Outline each uninfected red blood cell.
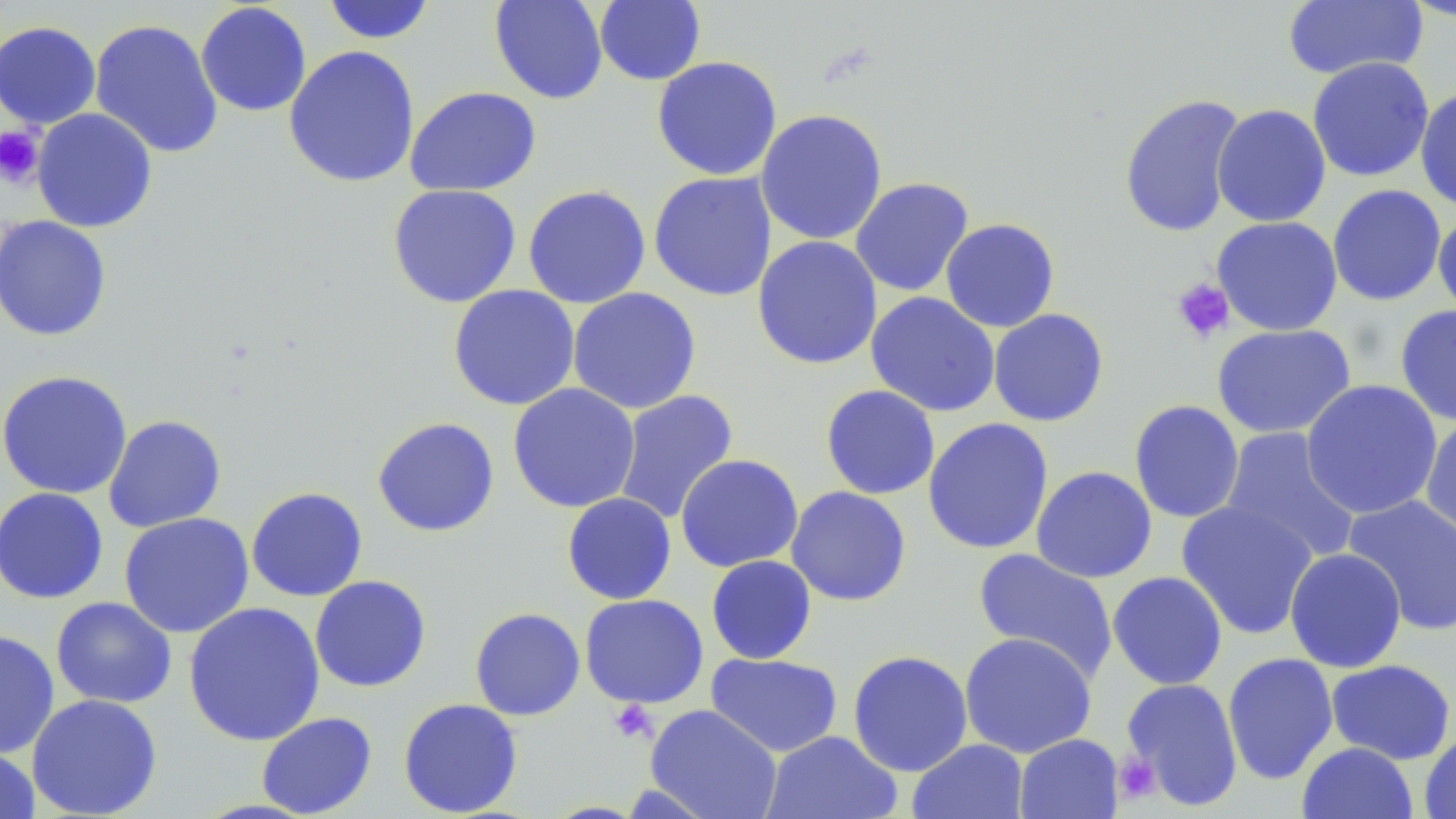

Approximate bounding boxes as (x1,y1)-(x2,y2) corner pairs in pixels.
Uninfected red blood cells: (321,0)-(437,44), (489,0)-(609,104), (595,0)-(706,85), (1398,0)-(1456,22), (1282,1)-(1427,81), (195,2)-(312,117), (89,18)-(224,159), (0,21)-(101,129), (283,45)-(420,189), (651,56)-(783,181), (1307,56)-(1434,183), (404,86)-(541,196), (1415,87)-(1456,213), (1118,93)-(1246,239), (1212,104)-(1331,227), (31,108)-(158,233), (755,109)-(888,246), (648,171)-(777,302), (849,177)-(974,297), (387,183)-(522,308), (1327,184)-(1447,306), (522,185)-(651,309), (1432,212)-(1456,320), (0,215)-(112,342), (1211,215)-(1343,336), (940,218)-(1060,332), (752,235)-(883,370), (448,285)-(580,411), (567,287)-(702,414), (865,291)-(1001,417), (1394,305)-(1456,426), (988,308)-(1109,427), (1211,323)-(1356,439), (0,370)-(133,500), (1300,379)-(1443,519), (507,383)-(641,513), (820,384)-(941,500), (613,389)-(739,525), (1129,399)-(1245,523), (103,414)-(227,533), (1420,414)-(1456,542), (371,416)-(500,537), (923,417)-(1054,555), (1219,427)-(1362,564), (675,454)-(804,573), (1031,465)-(1157,583), (246,486)-(368,602), (786,486)-(912,606), (0,487)-(109,605), (561,492)-(677,605), (1342,494)-(1456,636), (1176,500)-(1319,640), (118,512)-(255,638), (972,547)-(1120,682), (1284,548)-(1407,672), (705,555)-(817,664), (1107,571)-(1228,690), (309,575)-(432,693), (579,594)-(709,708), (51,596)-(177,708), (183,602)-(325,746), (469,607)-(586,721), (0,629)-(60,759), (959,632)-(1097,758), (847,649)-(973,777), (1222,652)-(1339,785), (705,653)-(843,758), (1325,659)-(1456,764), (1120,677)-(1244,811), (26,694)-(163,818), (398,698)-(524,817), (645,704)-(782,818), (256,712)-(378,818), (1419,729)-(1456,819), (761,730)-(903,819), (1015,733)-(1123,819), (908,738)-(1029,819), (1297,742)-(1418,819), (0,746)-(40,818).

slide-level diagnosis = no evidence of blood parasites
field of view = single
magnification = 1000x
image size = 1456×819 pixels
stain = May-Grünwald-Giemsa
modality = optical microscopy
platelet locations = approximate bounding boxes as (x1,y1)-(x2,y2) corner pairs in pixels: (0,125)-(45,189), (1171,278)-(1235,344), (607,699)-(657,744), (1113,750)-(1162,805)
preparation = thin blood smear